Locate every blood parasite and identify its species.
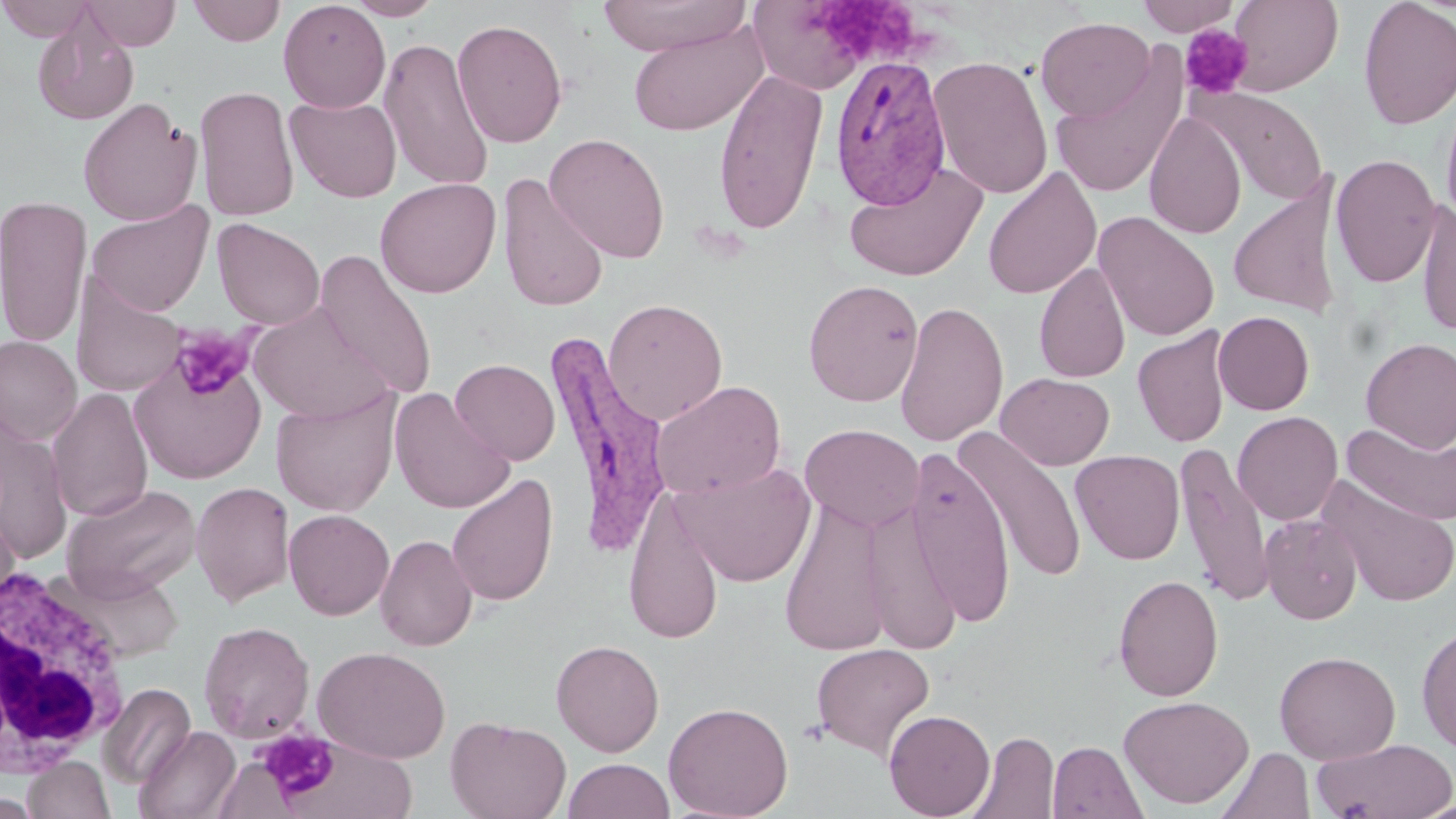
Approximate bounding boxes as (x1, y1, x2, y2) in pixels.
Plasmodium vivax-infected red blood cells: (830, 55, 951, 210), (545, 327, 675, 553).
No Plasmodium falciparum, Plasmodium ovale, Plasmodium malariae, Babesia divergens, or Trypanosoma brucei observed.

White blood cell locations: (0, 561, 131, 782). Uninfected red blood cell locations: (0, 0, 98, 41), (82, 0, 181, 50), (186, 0, 286, 46), (278, 0, 390, 113), (346, 0, 444, 20), (597, 0, 750, 57), (1228, 0, 1343, 96), (1357, 0, 1456, 130), (749, 1, 874, 94), (1137, 1, 1241, 36), (32, 15, 139, 127), (1036, 16, 1156, 121), (450, 18, 569, 147), (627, 20, 768, 137), (379, 36, 494, 192), (1050, 50, 1189, 200), (928, 54, 1053, 200), (713, 68, 828, 235), (195, 84, 300, 221), (1196, 90, 1330, 205), (1440, 91, 1456, 234), (284, 96, 403, 202), (77, 97, 202, 225), (1145, 110, 1247, 239), (544, 132, 670, 263), (1330, 153, 1442, 288), (843, 161, 988, 281), (982, 166, 1102, 300), (497, 174, 608, 313), (1228, 174, 1346, 319), (375, 177, 501, 298), (0, 195, 92, 348), (87, 200, 214, 317), (1416, 200, 1456, 337), (1093, 211, 1219, 342), (212, 218, 325, 330), (314, 248, 438, 400), (1034, 262, 1131, 383), (71, 271, 187, 398), (803, 279, 924, 406), (603, 298, 728, 425), (895, 300, 1009, 447), (249, 303, 391, 424), (1213, 311, 1314, 415), (1132, 326, 1232, 448), (0, 335, 82, 445), (1360, 337, 1456, 452), (129, 347, 267, 484), (450, 359, 560, 465), (995, 372, 1114, 470), (650, 380, 786, 500), (47, 388, 153, 522), (271, 388, 401, 517), (389, 388, 515, 514), (1232, 411, 1343, 525), (1341, 422, 1456, 528), (1, 423, 72, 567), (800, 423, 924, 531), (957, 430, 1087, 583), (1175, 441, 1275, 609), (904, 446, 1017, 629), (1071, 450, 1185, 565), (674, 462, 816, 588), (446, 473, 558, 608), (1316, 474, 1456, 608), (191, 481, 294, 607), (61, 483, 202, 599), (623, 486, 727, 646), (779, 497, 893, 657), (0, 499, 21, 614), (862, 499, 962, 654), (284, 509, 395, 620), (1260, 514, 1363, 624), (375, 534, 478, 651), (57, 566, 186, 663), (1113, 574, 1224, 701), (198, 620, 315, 742), (1416, 624, 1456, 754), (550, 639, 665, 757), (810, 643, 935, 761), (312, 646, 451, 763), (1274, 650, 1401, 764), (99, 682, 196, 789), (1118, 694, 1254, 809), (663, 701, 794, 819), (884, 709, 996, 819), (446, 716, 571, 819), (134, 725, 240, 819), (965, 731, 1059, 819), (277, 736, 419, 817), (1309, 738, 1456, 818), (1047, 741, 1147, 819), (1217, 747, 1315, 819), (21, 756, 115, 818), (561, 758, 675, 819), (0, 791, 45, 818), (1411, 799, 1456, 819). Platelet locations: (827, 3, 926, 61), (1179, 24, 1253, 99), (168, 323, 261, 401), (797, 718, 829, 747), (258, 729, 339, 802). Slide-level diagnosis: Plasmodium vivax. Thin blood smear. Light microscopy. Image is 1456×819 pixels. 1000x magnification. Single field of view. May-Grünwald-Giemsa-stained preparation.